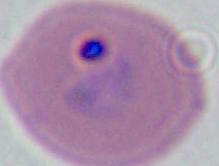

modality = photomicrograph
identification = Plasmodium
magnification = 400x or 1000x